Assess this cell for malaria.
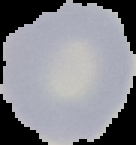

Uninfected.

image_size: 136×145 pixels
preparation: thin blood film
image_type: segmented cell region with the area outside set to black